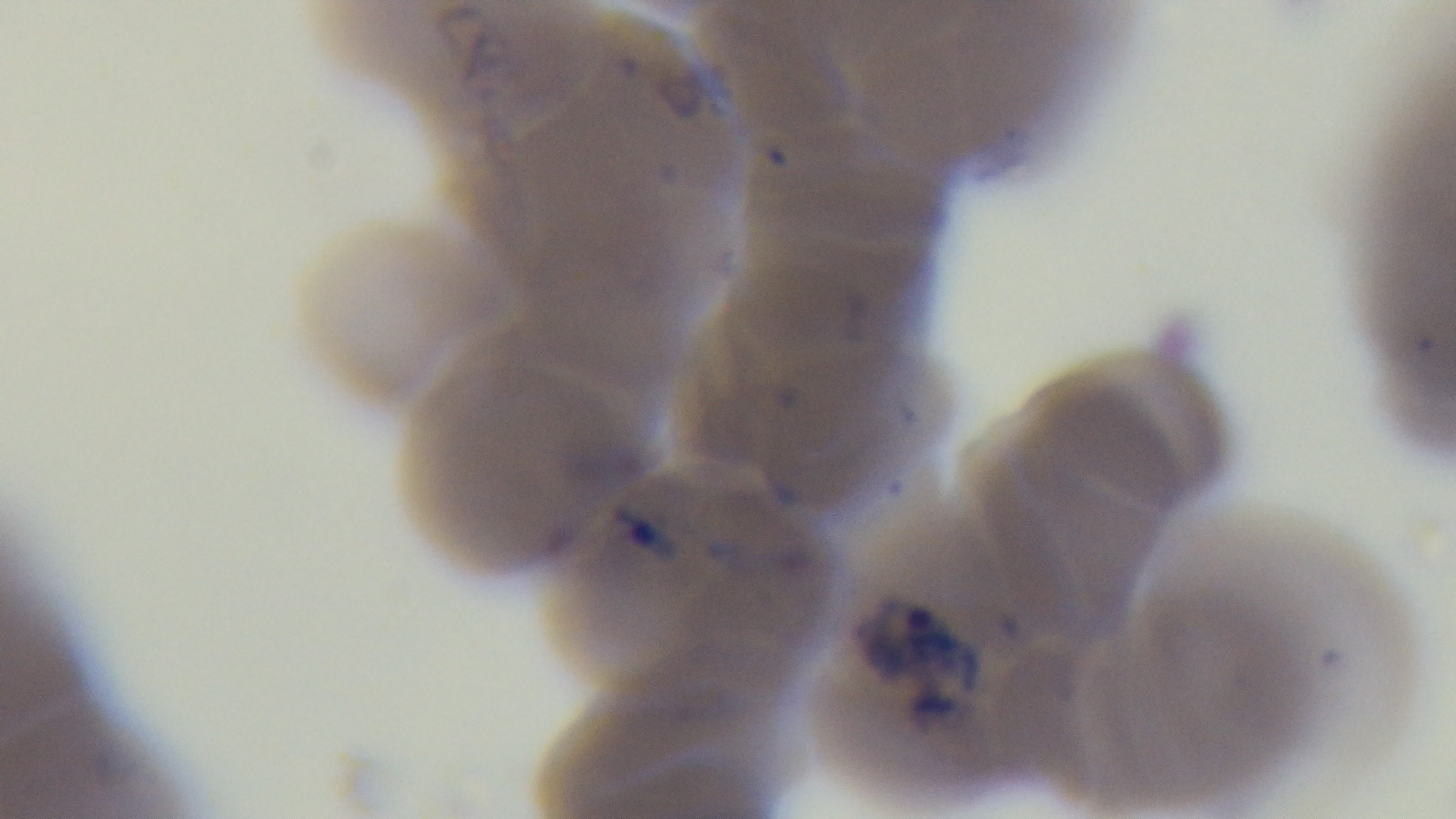

capture = mounted 4K digital camera
field of view = single
malaria status = positive
modality = light microscopy
objective = 100x oil immersion
stain = Giemsa
preparation = thin